Point out each Plasmodium parasite.
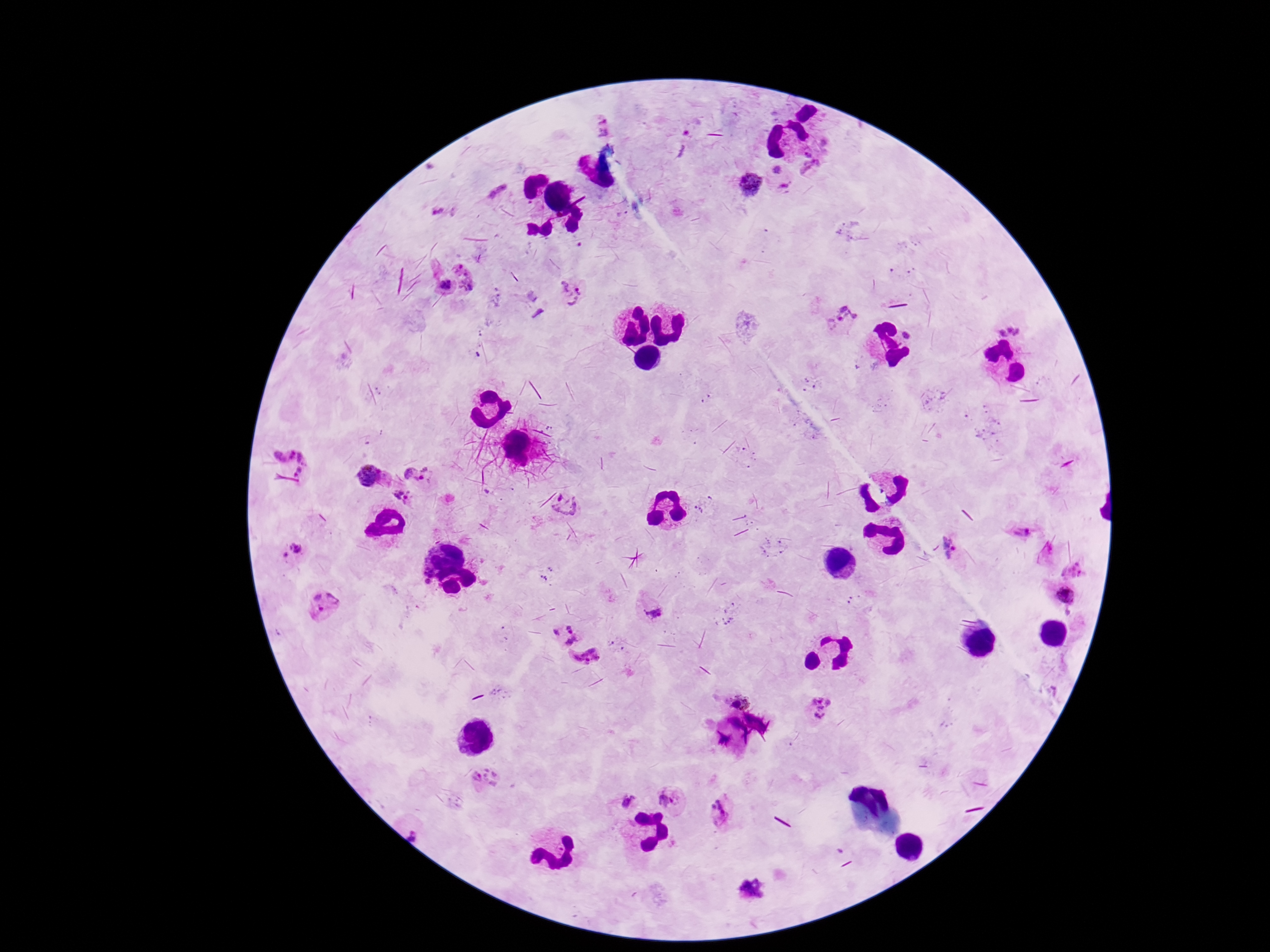
Approximate centers as {x, y} in pixels.
Plasmodium parasites: {603, 124}, {813, 169}, {778, 170}, {750, 184}, {498, 188}, {437, 210}, {468, 276}, {446, 286}, {571, 291}, {842, 319}, {1010, 326}, {908, 334}, {299, 448}, {371, 474}, {419, 475}, {402, 500}, {566, 504}, {1024, 525}, {949, 546}, {291, 549}, {1064, 596}, {325, 606}, {653, 610}, {565, 634}, {586, 656}, {733, 692}, {821, 707}, {484, 777}, {672, 799}, {626, 800}, {722, 812}, {416, 832}.

Summary:
  - Image size: 1270×952 pixels
  - Magnification: 100x
  - Patient malaria status: infected
  - Field of view: one from this slide
  - Preparation: thick peripheral-blood smear
  - Stain: Giemsa
  - Capture: smartphone camera through the microscope eyepiece